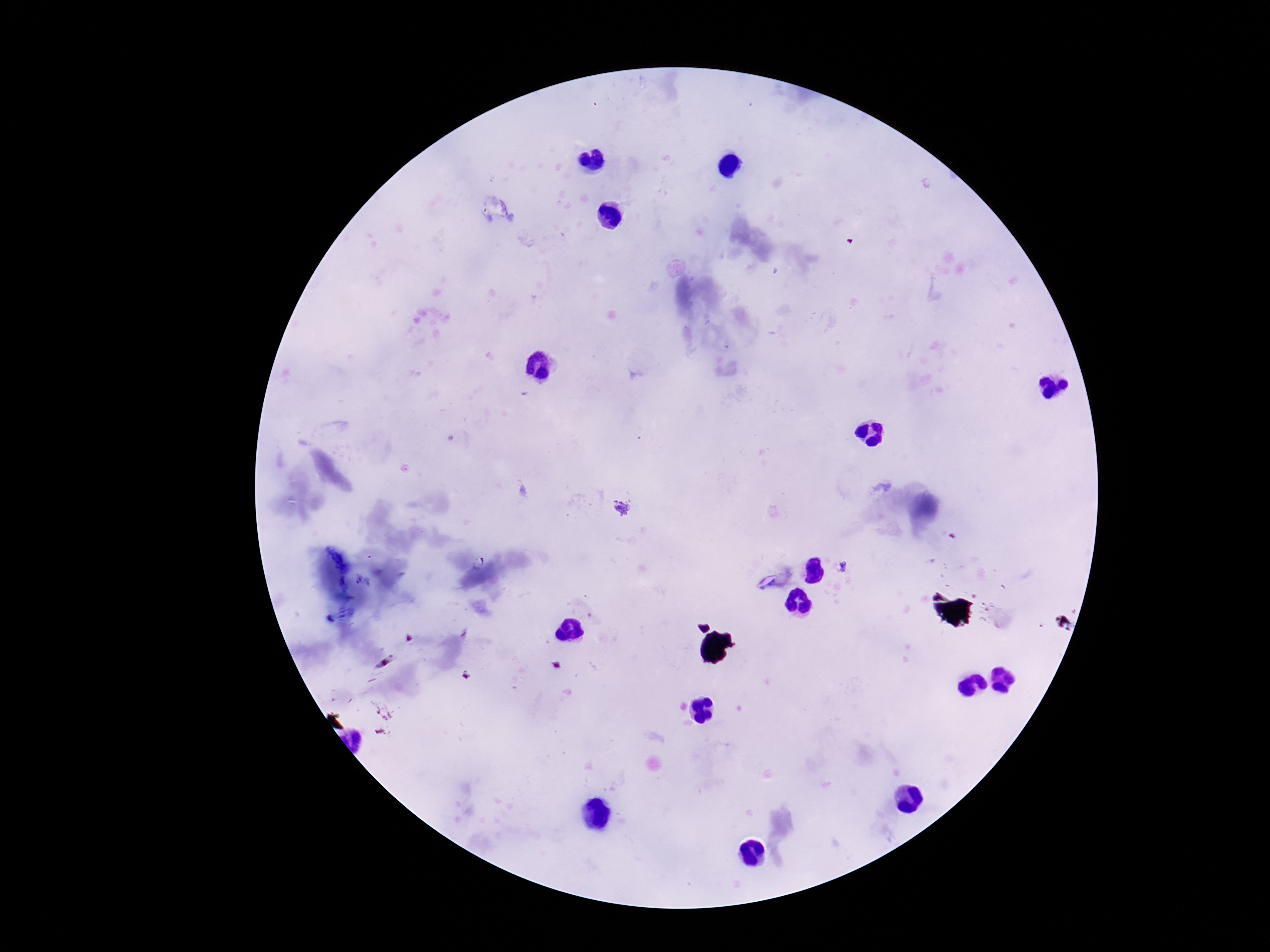
Approximate object centers, in pixels from the top-left corner.
Summary:
  - Plasmodium parasite locations: (x=625, y=507), (x=844, y=567)
  - Magnification: 100x
  - Image size: 1270×952 pixels
  - Capture: smartphone camera through the microscope eyepiece
  - Preparation: thick blood film
  - Stain: Giemsa
  - Patient malaria status: positive
  - Field of view: single